Locate every blood parasite and identify its species.
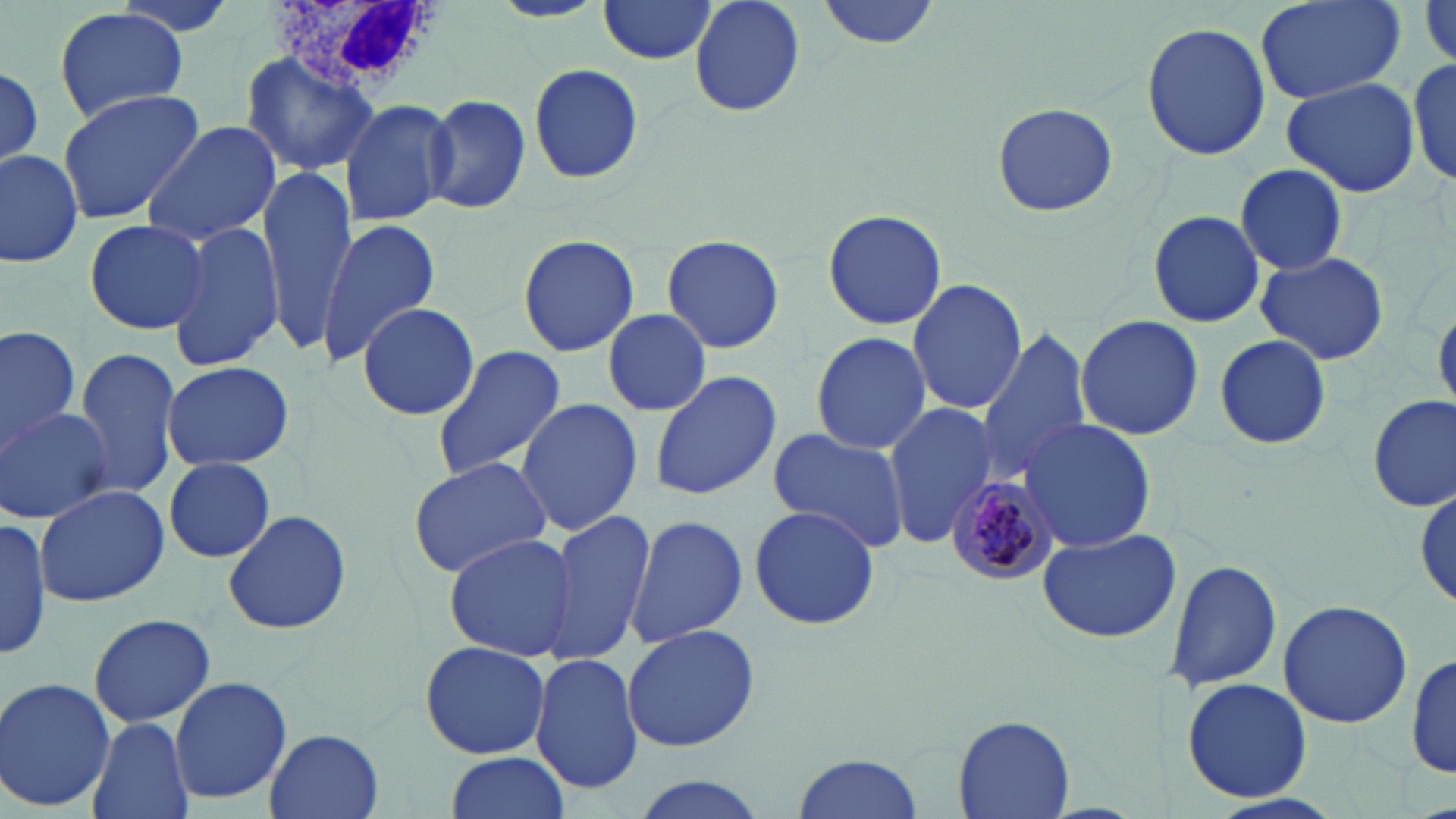
Approximate bounding boxes as named x1/y1/x2/y2 corners in pixels.
Plasmodium malariae-infected red blood cells: (x1=941, y1=474, x2=1061, y2=587).
No Plasmodium falciparum, Plasmodium ovale, Plasmodium vivax, Babesia divergens, or Trypanosoma brucei observed.

Uninfected red blood cell locations: (x1=488, y1=0, x2=607, y2=24), (x1=690, y1=0, x2=805, y2=119), (x1=817, y1=0, x2=944, y2=50), (x1=1255, y1=0, x2=1405, y2=106), (x1=596, y1=1, x2=719, y2=66), (x1=1418, y1=4, x2=1456, y2=70), (x1=52, y1=8, x2=190, y2=125), (x1=1141, y1=21, x2=1271, y2=160), (x1=241, y1=52, x2=378, y2=175), (x1=1409, y1=57, x2=1456, y2=188), (x1=528, y1=61, x2=646, y2=185), (x1=0, y1=65, x2=44, y2=170), (x1=1282, y1=76, x2=1421, y2=197), (x1=56, y1=89, x2=204, y2=225), (x1=426, y1=95, x2=531, y2=213), (x1=338, y1=97, x2=455, y2=227), (x1=990, y1=102, x2=1119, y2=216), (x1=141, y1=119, x2=282, y2=246), (x1=1, y1=148, x2=83, y2=267), (x1=1234, y1=163, x2=1349, y2=276), (x1=259, y1=168, x2=358, y2=349), (x1=820, y1=207, x2=949, y2=332), (x1=1148, y1=211, x2=1268, y2=329), (x1=82, y1=217, x2=211, y2=336), (x1=319, y1=219, x2=440, y2=364), (x1=168, y1=223, x2=286, y2=371), (x1=517, y1=233, x2=639, y2=357), (x1=660, y1=234, x2=786, y2=354), (x1=1253, y1=252, x2=1390, y2=365), (x1=907, y1=278, x2=1028, y2=417), (x1=356, y1=302, x2=479, y2=422), (x1=603, y1=308, x2=711, y2=418), (x1=1074, y1=314, x2=1204, y2=441), (x1=1, y1=324, x2=82, y2=455), (x1=976, y1=329, x2=1093, y2=478), (x1=811, y1=330, x2=933, y2=457), (x1=1214, y1=334, x2=1331, y2=453), (x1=430, y1=344, x2=568, y2=482), (x1=73, y1=350, x2=181, y2=499), (x1=160, y1=361, x2=296, y2=471), (x1=649, y1=370, x2=781, y2=502), (x1=1367, y1=394, x2=1454, y2=515), (x1=515, y1=396, x2=644, y2=537), (x1=881, y1=402, x2=996, y2=546), (x1=1, y1=407, x2=115, y2=524), (x1=1020, y1=420, x2=1157, y2=552), (x1=766, y1=429, x2=915, y2=554), (x1=406, y1=456, x2=554, y2=579), (x1=164, y1=457, x2=275, y2=563), (x1=36, y1=482, x2=167, y2=609), (x1=1414, y1=484, x2=1453, y2=613), (x1=748, y1=503, x2=883, y2=632), (x1=223, y1=506, x2=352, y2=636), (x1=544, y1=510, x2=657, y2=664), (x1=625, y1=514, x2=746, y2=649), (x1=0, y1=516, x2=52, y2=662), (x1=1038, y1=527, x2=1182, y2=643), (x1=443, y1=533, x2=580, y2=663), (x1=1165, y1=559, x2=1282, y2=692), (x1=1277, y1=600, x2=1415, y2=730), (x1=86, y1=613, x2=218, y2=727), (x1=620, y1=623, x2=762, y2=753), (x1=418, y1=641, x2=552, y2=759), (x1=1411, y1=648, x2=1454, y2=782), (x1=530, y1=653, x2=644, y2=796), (x1=1181, y1=676, x2=1313, y2=804), (x1=0, y1=678, x2=118, y2=812), (x1=169, y1=678, x2=292, y2=804), (x1=946, y1=712, x2=1074, y2=818), (x1=87, y1=716, x2=192, y2=819), (x1=264, y1=728, x2=383, y2=819), (x1=442, y1=752, x2=572, y2=819), (x1=791, y1=752, x2=924, y2=819), (x1=628, y1=775, x2=775, y2=819). White blood cell locations: (x1=263, y1=0, x2=443, y2=98). Slide-level diagnosis: Plasmodium malariae. Captured at 1000x magnification. Light microscopy. Thin blood smear. Single field of view. May-Grünwald-Giemsa stain. Image is 1456×819 pixels.